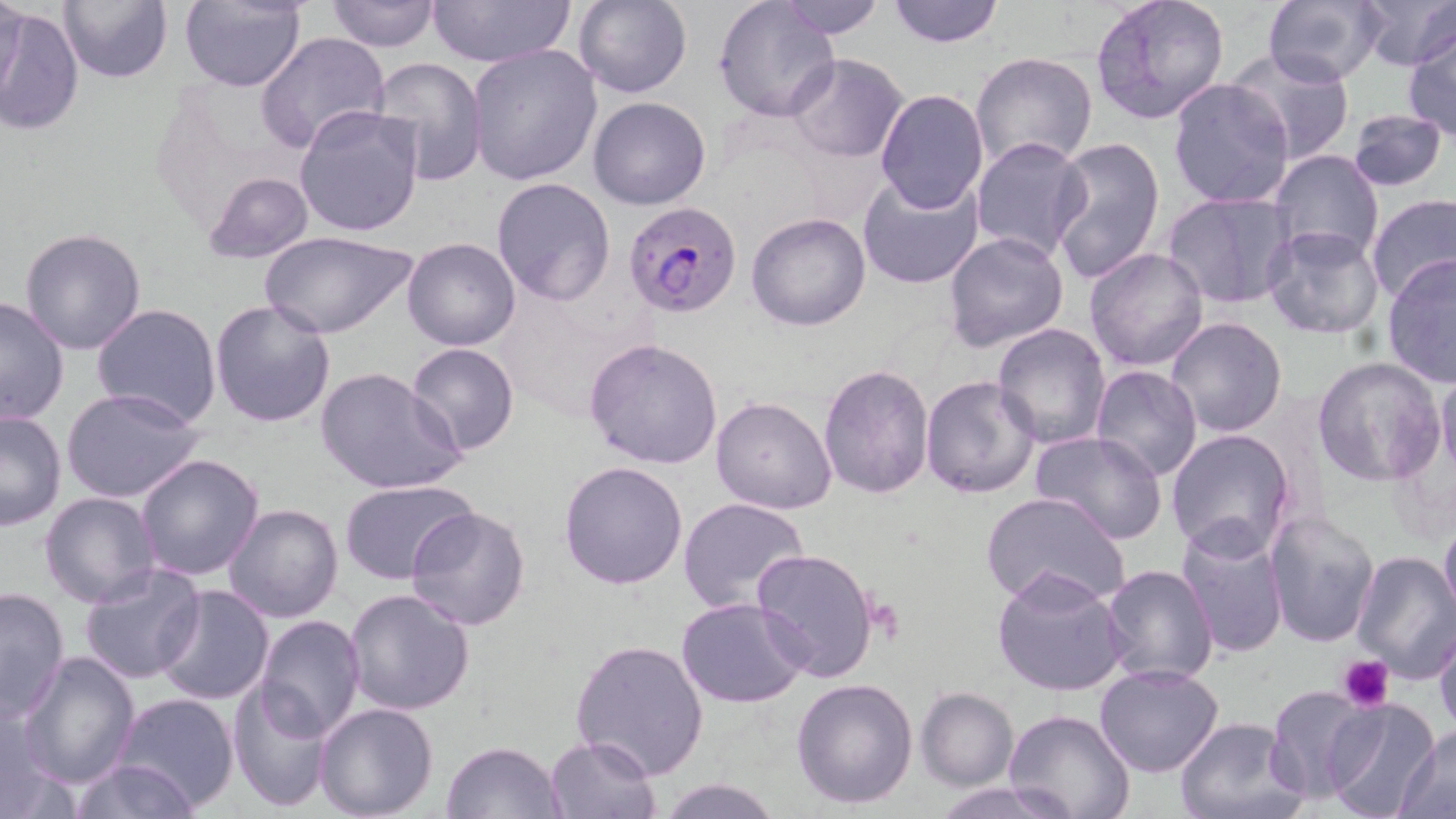
{
  "slide_level_diagnosis": "Plasmodium falciparum",
  "magnification": "1000x",
  "uninfected_red_blood_cell_locations": "approximate bounding boxes as [x1, y1, x2, y2] in pixels: [0, 0, 26, 117], [58, 0, 173, 83], [324, 0, 440, 51], [427, 0, 576, 70], [572, 0, 692, 99], [714, 0, 838, 121], [776, 0, 889, 38], [886, 0, 1003, 47], [1090, 0, 1230, 126], [1356, 0, 1456, 71], [180, 1, 307, 92], [1263, 2, 1387, 86], [2, 6, 83, 137], [1402, 22, 1456, 141], [255, 32, 389, 153], [467, 43, 603, 186], [1227, 47, 1356, 164], [970, 52, 1097, 173], [787, 54, 910, 162], [372, 57, 488, 183], [1167, 78, 1296, 210], [875, 88, 989, 214], [588, 96, 710, 210], [293, 103, 425, 236], [1348, 109, 1448, 190], [969, 136, 1091, 263], [1050, 136, 1167, 283], [1269, 148, 1385, 263], [200, 171, 316, 265], [858, 172, 985, 289], [491, 177, 616, 306], [1161, 191, 1299, 310], [1365, 192, 1456, 303], [746, 212, 871, 332], [1261, 225, 1385, 339], [19, 228, 147, 355], [259, 230, 417, 340], [943, 231, 1070, 354], [402, 237, 521, 351], [1085, 248, 1209, 371], [1382, 255, 1456, 386], [0, 295, 71, 426], [210, 299, 337, 427], [90, 303, 222, 430], [1165, 316, 1288, 439], [993, 323, 1110, 448], [584, 338, 725, 469], [407, 342, 520, 457], [1313, 356, 1446, 488], [818, 362, 935, 502], [316, 366, 466, 497], [1089, 366, 1205, 482], [1436, 373, 1456, 478], [920, 375, 1040, 500], [62, 387, 206, 503], [710, 395, 837, 514], [0, 410, 66, 532], [1165, 429, 1296, 562], [1030, 431, 1172, 546], [136, 455, 264, 580], [558, 459, 690, 590], [339, 479, 481, 582], [40, 491, 163, 609], [981, 491, 1129, 609], [677, 498, 811, 614], [224, 503, 344, 622], [405, 505, 530, 631], [1266, 510, 1382, 650], [1439, 514, 1456, 627], [1174, 523, 1290, 661], [750, 547, 881, 684], [1351, 550, 1456, 682], [76, 561, 204, 684], [1098, 562, 1218, 686], [991, 567, 1131, 698], [153, 583, 275, 704], [0, 586, 72, 721], [344, 589, 475, 716], [677, 598, 807, 708], [255, 615, 366, 739], [1433, 625, 1456, 737], [570, 638, 709, 780], [18, 650, 140, 789], [1093, 664, 1224, 777], [791, 677, 920, 809], [227, 682, 335, 813], [1265, 685, 1374, 802], [915, 687, 1018, 789], [112, 692, 239, 814], [0, 698, 68, 819], [1322, 698, 1442, 818], [314, 702, 439, 819], [1002, 709, 1134, 819], [1176, 716, 1306, 819], [1398, 727, 1455, 817], [545, 734, 660, 818], [443, 740, 566, 818], [65, 758, 201, 819], [656, 777, 784, 818], [930, 781, 1076, 819]",
  "preparation": "thin blood smear",
  "plasmodium_falciparum_infected_red_blood_cell_locations": "approximate bounding boxes as [x1, y1, x2, y2] in pixels: [623, 202, 744, 316]",
  "modality": "light microscopy",
  "image_size": "1456×819 pixels",
  "stain": "May-Grünwald-Giemsa",
  "platelet_locations": "approximate bounding boxes as [x1, y1, x2, y2] in pixels: [1339, 654, 1395, 711]",
  "field_of_view": "one of a larger specimen"
}